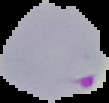
image size = 109×103 pixels
image type = segmented cell region on a black background
result = malaria parasites identified
preparation = thin blood film